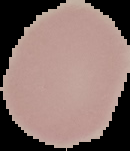

Summary:
  - Preparation: thin blood film
  - Image size: 130×151 pixels
  - Result: no malaria parasites seen
  - Image type: cell region segmented out of the field of view; surrounding area masked to black